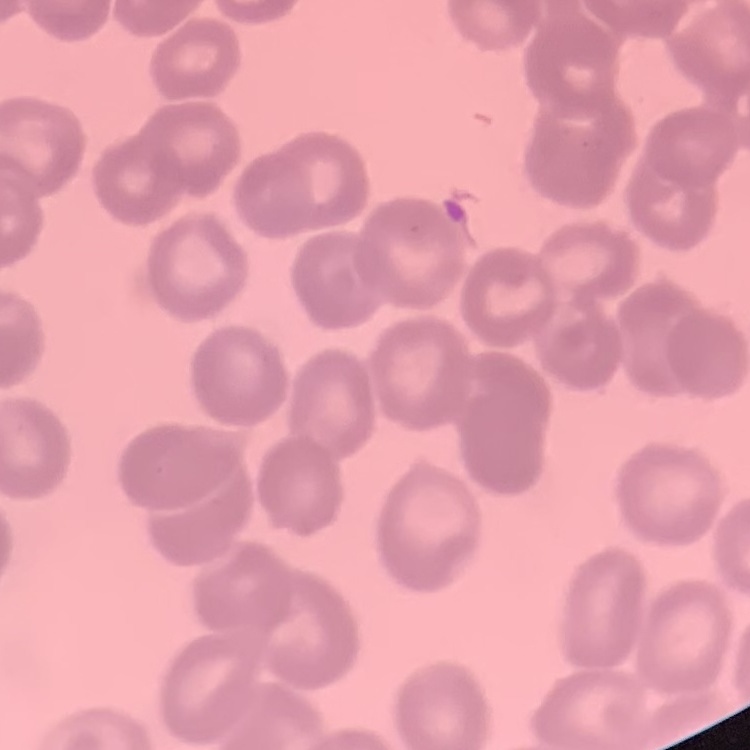
erythrocyte_morphology: rouleaux formation
preparation: thin peripheral smear
stain: Field's or Giemsa
image_type: one tile cut from a larger photomicrograph